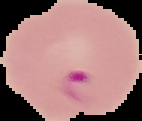

From a thin blood smear. Malaria status: parasitized. Image is 142×121 pixels. Segmented cell region on a black background.